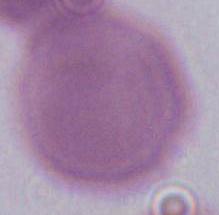

identification: erythrocyte
modality: photomicrograph
magnification: 1000x